Assess this cell for malaria.
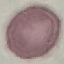
Uninfected.

Summary:
  - Capture: smartphone camera at the microscope eyepiece
  - Image type: automatically extracted cell patch, resized to 64 × 64 pixels
  - Stain: Giemsa
  - Preparation: thin blood smear